Give the position of every malaria parasite.
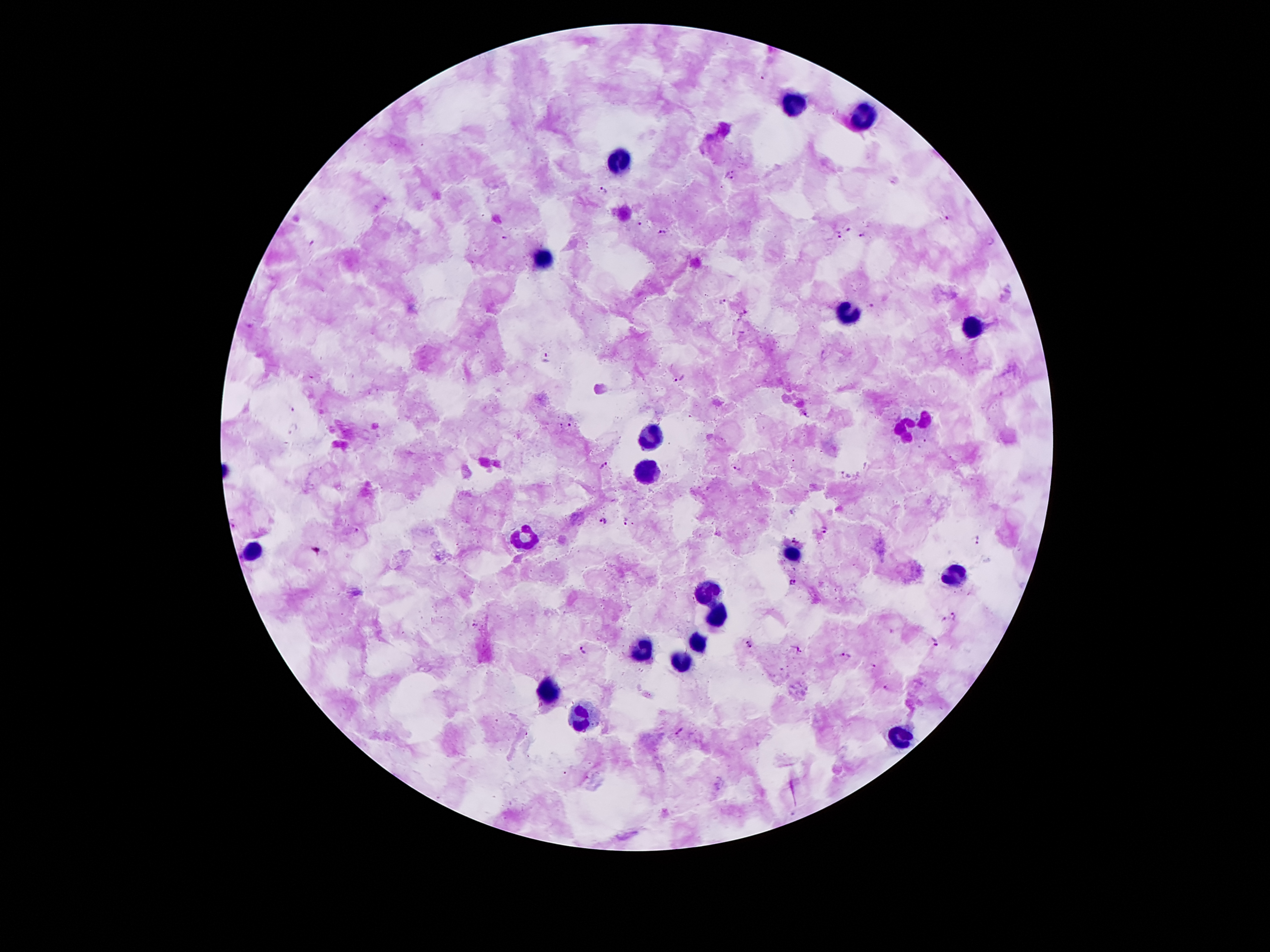
Approximate centers as (x, y) in pixels.
Malaria parasites: (731, 175), (603, 189), (950, 218), (640, 222), (850, 228), (662, 230), (863, 235), (839, 236), (505, 237), (314, 241), (991, 242), (722, 302), (871, 307), (746, 313), (547, 357), (681, 377), (570, 425), (293, 429), (604, 464), (738, 468), (845, 475), (602, 520), (626, 521), (356, 530), (823, 531), (795, 539), (977, 539), (793, 581), (954, 616), (944, 621), (476, 625), (936, 641), (748, 644), (798, 649), (583, 650), (847, 655), (874, 666), (885, 688), (680, 729).

Summary:
  - Leukocyte locations: (792, 99), (862, 116), (622, 157), (540, 260), (847, 311), (973, 327), (926, 419), (905, 430), (650, 435), (645, 469), (526, 537), (253, 548), (793, 554), (961, 573), (709, 589), (718, 613), (696, 638), (646, 646), (682, 661), (550, 695), (581, 718), (900, 739)
  - Image size: 1270×952 pixels
  - Magnification: 100x
  - Patient malaria status: infected with Plasmodium falciparum
  - Stain: Giemsa
  - Field of view: single
  - Preparation: thick blood smear
  - Capture: smartphone through the microscope eyepiece